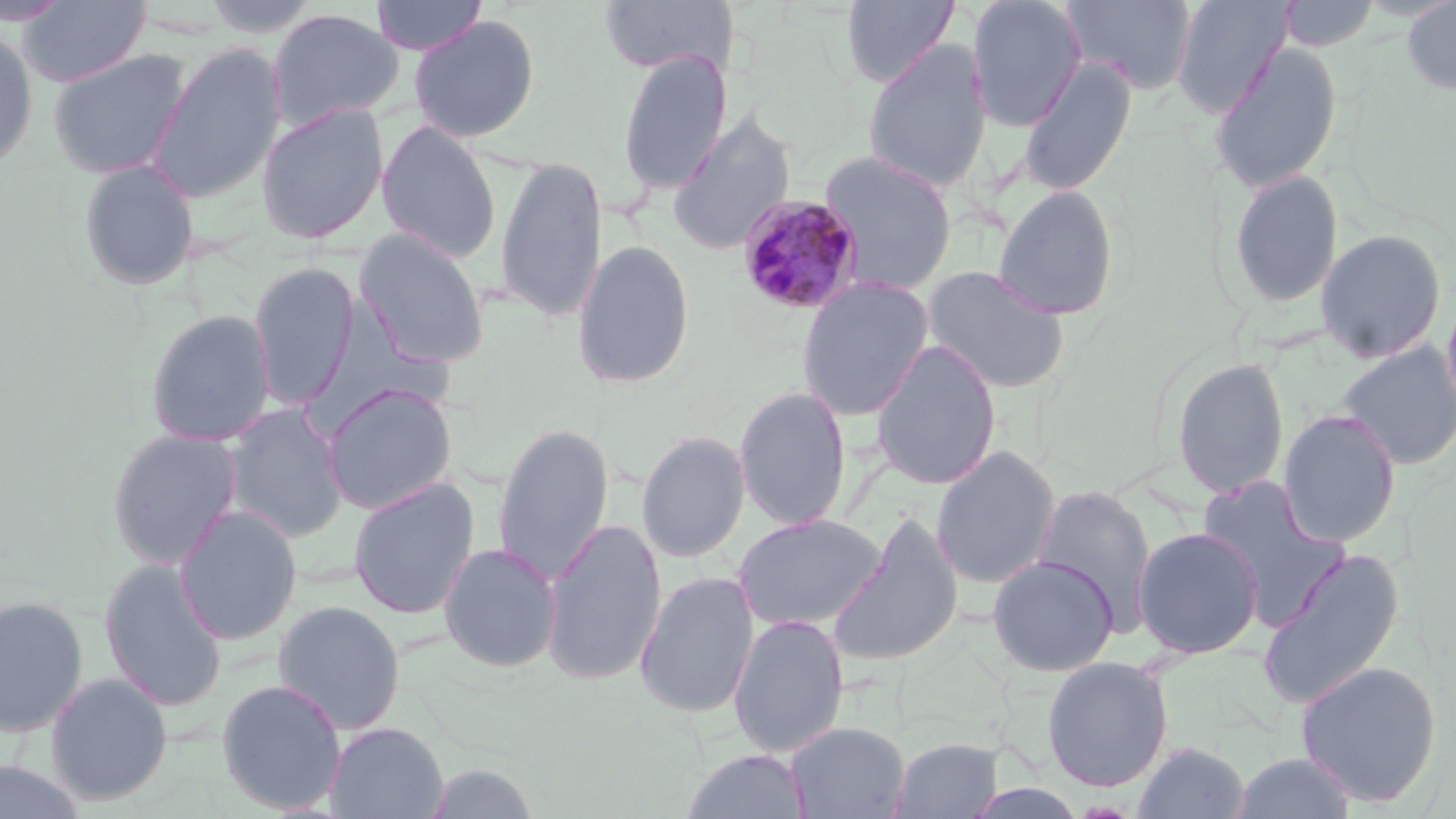

Summary:
  - Coordinate format: approximate bounding boxes as (x1, y1, x2, y2) in pixels
  - Uninfected red blood cell locations: (18, 0, 152, 88), (200, 0, 323, 38), (370, 0, 488, 56), (598, 0, 738, 77), (841, 0, 960, 88), (966, 0, 1087, 132), (1062, 0, 1198, 96), (1171, 0, 1293, 117), (1276, 0, 1380, 50), (1401, 0, 1456, 95), (0, 1, 74, 26), (267, 8, 404, 130), (408, 14, 541, 143), (0, 27, 38, 173), (862, 38, 993, 195), (149, 42, 286, 203), (1210, 43, 1342, 194), (617, 48, 733, 195), (48, 49, 191, 180), (1017, 56, 1137, 195), (255, 103, 389, 245), (667, 112, 797, 254), (376, 121, 501, 263), (818, 150, 958, 295), (493, 155, 607, 324), (76, 158, 200, 291), (1227, 170, 1344, 311), (993, 185, 1120, 320), (353, 228, 490, 369), (1315, 229, 1447, 363), (571, 239, 695, 389), (248, 261, 360, 412), (922, 265, 1070, 394), (796, 277, 933, 421), (145, 309, 276, 447), (870, 338, 1002, 490), (1336, 343, 1456, 470), (1171, 357, 1289, 499), (321, 383, 458, 515), (733, 385, 852, 531), (221, 404, 349, 543), (1277, 409, 1402, 548), (493, 422, 614, 585), (106, 427, 243, 570), (637, 430, 751, 563), (931, 446, 1060, 590), (1196, 474, 1349, 627), (347, 478, 480, 620), (1031, 485, 1157, 633), (174, 505, 303, 646), (732, 513, 888, 633), (827, 513, 964, 669), (540, 518, 667, 686), (1131, 526, 1264, 659), (439, 543, 561, 673), (1257, 547, 1405, 709), (986, 554, 1119, 676), (98, 558, 229, 712), (634, 571, 759, 718), (0, 594, 89, 738), (272, 600, 406, 734), (728, 614, 849, 757), (1041, 656, 1174, 792), (1295, 660, 1442, 807), (44, 672, 174, 806), (216, 679, 347, 815), (786, 721, 910, 819), (325, 722, 449, 818), (888, 737, 1005, 818), (1132, 741, 1250, 819), (681, 748, 811, 818), (1228, 752, 1359, 818), (0, 760, 89, 819), (419, 760, 543, 819)
  - Plasmodium malariae-infected red blood cell locations: (736, 195, 864, 315)
  - Slide-level diagnosis: Plasmodium malariae
  - Image size: 1456×819 pixels
  - Preparation: thin blood film
  - Stain: May-Grünwald-Giemsa
  - Field of view: one of a larger specimen
  - Modality: optical microscopy
  - Magnification: 1000x